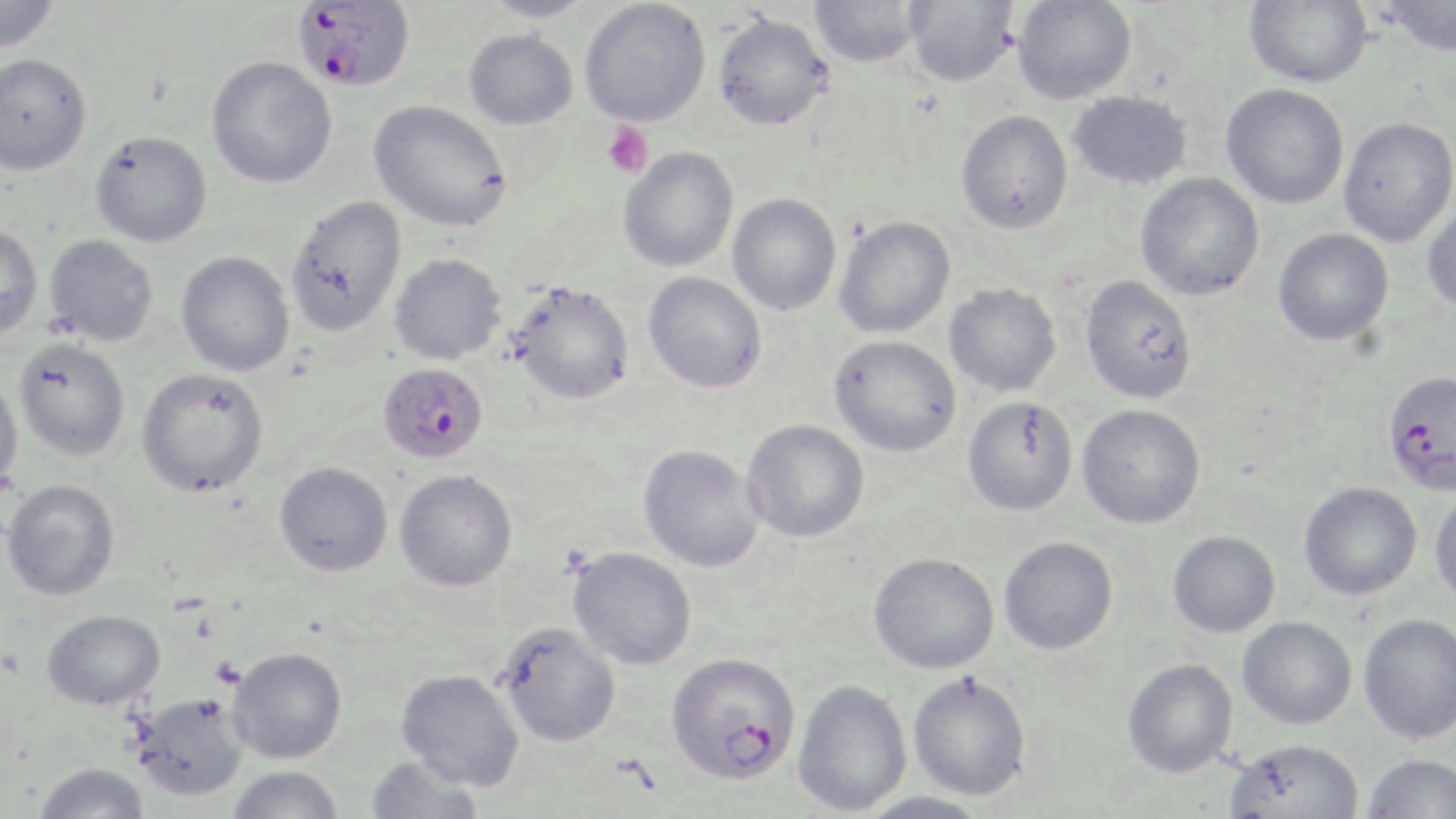
Summary:
  - Coordinate format: approximate bounding boxes as [x1, y1, x2, y2] in pixels
  - Platelet locations: [602, 121, 653, 179]
  - Uninfected red blood cell locations: [0, 0, 60, 55], [481, 0, 594, 22], [1012, 0, 1136, 104], [1243, 0, 1372, 88], [1378, 0, 1456, 58], [579, 1, 711, 127], [809, 1, 923, 68], [904, 1, 1020, 87], [712, 12, 833, 131], [463, 29, 577, 130], [0, 54, 93, 176], [206, 55, 337, 188], [1221, 84, 1349, 209], [1067, 91, 1192, 191], [369, 100, 512, 232], [955, 110, 1073, 234], [1338, 117, 1456, 247], [90, 131, 212, 248], [618, 147, 739, 272], [1135, 173, 1264, 301], [727, 194, 841, 315], [285, 196, 407, 338], [1421, 196, 1456, 311], [833, 215, 955, 339], [0, 222, 44, 341], [1273, 228, 1393, 346], [45, 234, 158, 346], [176, 252, 294, 376], [389, 253, 507, 365], [642, 272, 767, 393], [1079, 275, 1197, 404], [508, 281, 634, 405], [944, 283, 1061, 397], [829, 335, 961, 457], [14, 339, 131, 460], [136, 367, 269, 497], [0, 373, 23, 493], [962, 396, 1078, 516], [1077, 404, 1206, 529], [741, 420, 869, 543], [639, 445, 764, 572], [274, 461, 393, 576], [394, 469, 518, 592], [2, 479, 120, 601], [1298, 482, 1422, 600], [1429, 486, 1456, 609], [1167, 530, 1280, 638], [998, 536, 1117, 655], [567, 546, 697, 670], [869, 552, 999, 674], [42, 608, 165, 710], [1358, 614, 1456, 744], [1237, 616, 1357, 730], [496, 622, 620, 747], [227, 647, 347, 764], [1122, 658, 1238, 778], [396, 668, 524, 790], [907, 671, 1032, 801], [792, 679, 912, 815], [133, 693, 248, 801], [1225, 739, 1365, 819], [1361, 753, 1456, 818], [364, 756, 485, 819], [34, 762, 150, 819], [226, 765, 345, 819], [855, 791, 991, 819]
  - Plasmodium falciparum-infected red blood cell locations: [294, 1, 415, 93], [377, 362, 489, 464], [1382, 369, 1455, 494], [665, 651, 801, 784]
  - Slide-level diagnosis: Plasmodium falciparum
  - Preparation: thin blood smear
  - Field of view: one of a larger specimen
  - Image size: 1456×819 pixels
  - Magnification: 1000x
  - Stain: May-Grünwald-Giemsa
  - Modality: light microscopy